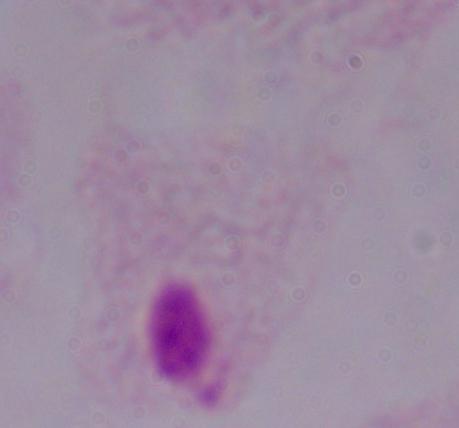

A trichomonad is shown. 1000x magnification. Micrograph.